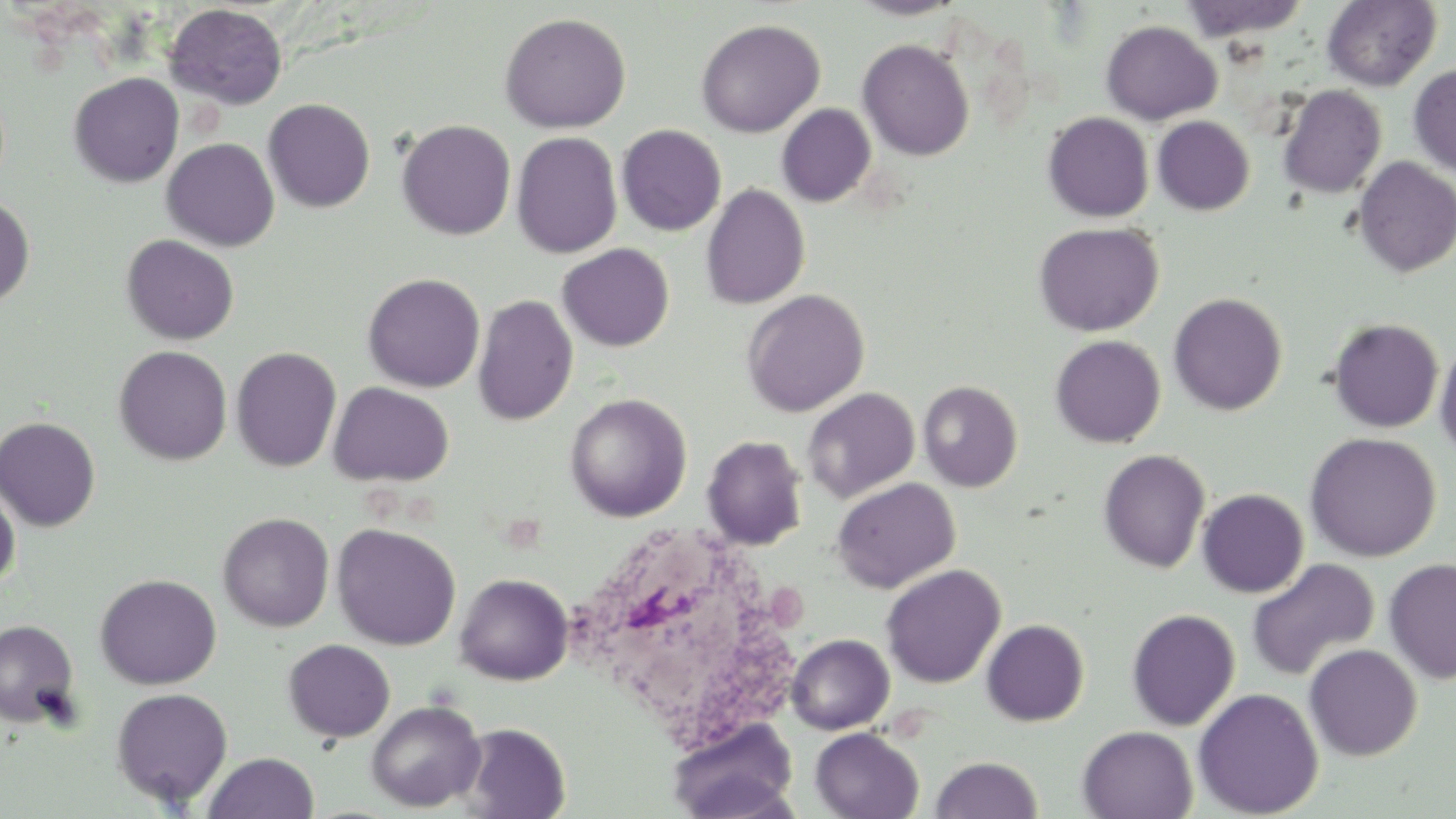

Summary:
  - Coordinate format: approximate bounding boxes as (x1,y1)-(x2,y2) corner pairs in pixels
  - White blood cell locations: (563,519)-(799,757)
  - Uninfected red blood cell locations: (847,0)-(968,20), (1179,0)-(1311,42), (1322,0)-(1441,91), (164,3)-(288,110), (498,12)-(631,134), (694,18)-(826,138), (1100,20)-(1221,124), (857,39)-(974,161), (1408,63)-(1456,176), (68,72)-(184,188), (1278,84)-(1386,199), (263,98)-(375,213), (776,103)-(876,207), (1043,112)-(1154,222), (1152,116)-(1254,215), (396,119)-(516,241), (616,124)-(726,236), (511,132)-(622,259), (162,137)-(280,252), (1353,156)-(1456,277), (700,184)-(810,309), (0,195)-(35,308), (1033,221)-(1164,337), (121,234)-(239,345), (557,243)-(674,351), (362,273)-(485,392), (742,288)-(869,417), (1168,292)-(1287,415), (472,294)-(578,425), (1328,318)-(1444,433), (1050,334)-(1166,447), (1434,335)-(1456,460), (114,345)-(232,465), (231,347)-(342,472), (918,381)-(1022,492), (328,382)-(454,487), (802,388)-(920,504), (564,393)-(692,522), (0,416)-(101,532), (1304,432)-(1441,562), (702,435)-(807,550), (1098,449)-(1211,573), (831,477)-(960,594), (0,482)-(20,590), (1197,488)-(1309,598), (218,512)-(334,631), (331,522)-(461,650), (1246,558)-(1380,682), (1383,558)-(1456,685), (880,564)-(1005,688), (94,573)-(222,690), (454,573)-(573,685), (1125,608)-(1240,731), (981,619)-(1089,726), (0,620)-(80,727), (787,634)-(894,735), (802,634)-(909,819), (283,639)-(395,742), (1304,644)-(1422,761), (111,687)-(233,808), (1192,688)-(1323,818), (366,700)-(485,812), (666,718)-(799,819), (457,723)-(571,818), (1077,726)-(1198,819), (810,728)-(924,818), (203,752)-(319,819), (930,756)-(1043,818)
  - Slide-level diagnosis: negative for blood parasites
  - Magnification: 1000x
  - Stain: May-Grünwald-Giemsa
  - Image size: 1456×819 pixels
  - Modality: light microscopy
  - Preparation: thin blood smear
  - Field of view: one of a larger specimen